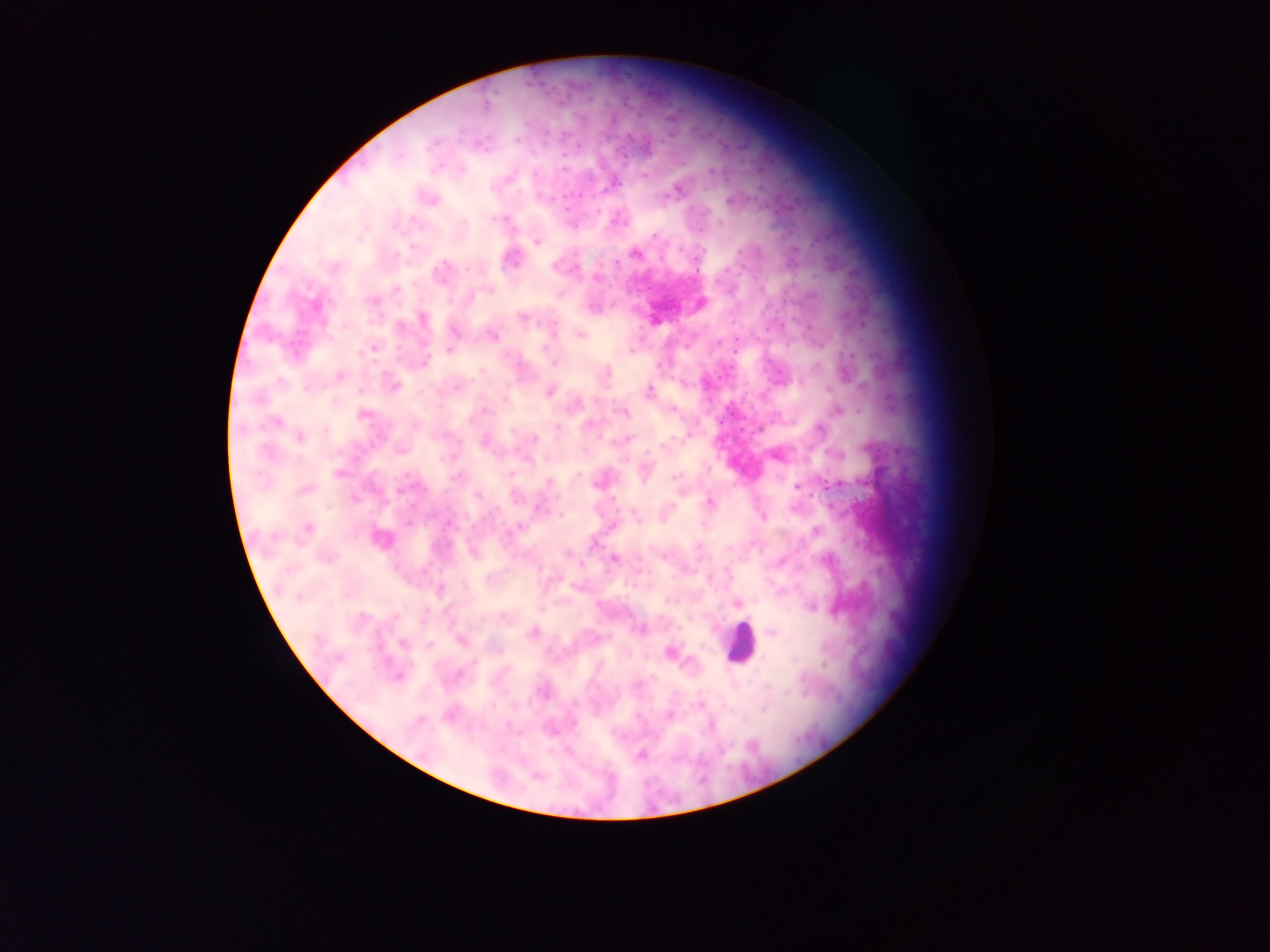
Approximate centers as (x, y) in pixels.
Summary:
  - Leukocyte locations: (739, 643)
  - Malaria parasite locations: (461, 170), (429, 199), (731, 201), (537, 241), (634, 253), (510, 258), (334, 267), (440, 273), (699, 303), (422, 318), (579, 334), (492, 335), (372, 347), (449, 349), (630, 350), (423, 362), (339, 376), (392, 385), (549, 391), (649, 391), (838, 409), (622, 411), (363, 415), (275, 422), (300, 436), (484, 441), (401, 449), (776, 454), (645, 469), (338, 472), (457, 477), (600, 480), (549, 482), (797, 486), (304, 489), (478, 495), (710, 503), (538, 507), (763, 517), (613, 525), (306, 529), (815, 531), (379, 538), (473, 552), (614, 558), (737, 603), (810, 606), (639, 629), (533, 632), (771, 632), (462, 640), (671, 652), (398, 676), (543, 691), (668, 715), (640, 755)
  - Preparation: thick blood film
  - Field of view: single
  - Image size: 1270×952 pixels
  - Country: Ghana
  - Capture: mobile-phone photograph through a microscope